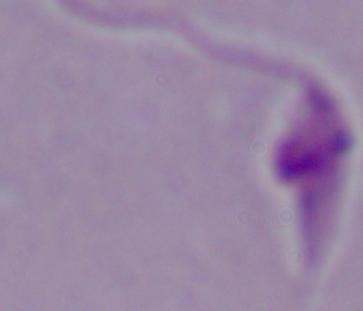
Photomicrograph. A Leishmania parasite is shown. Captured at 1000x magnification.